Name the blood parasite species.
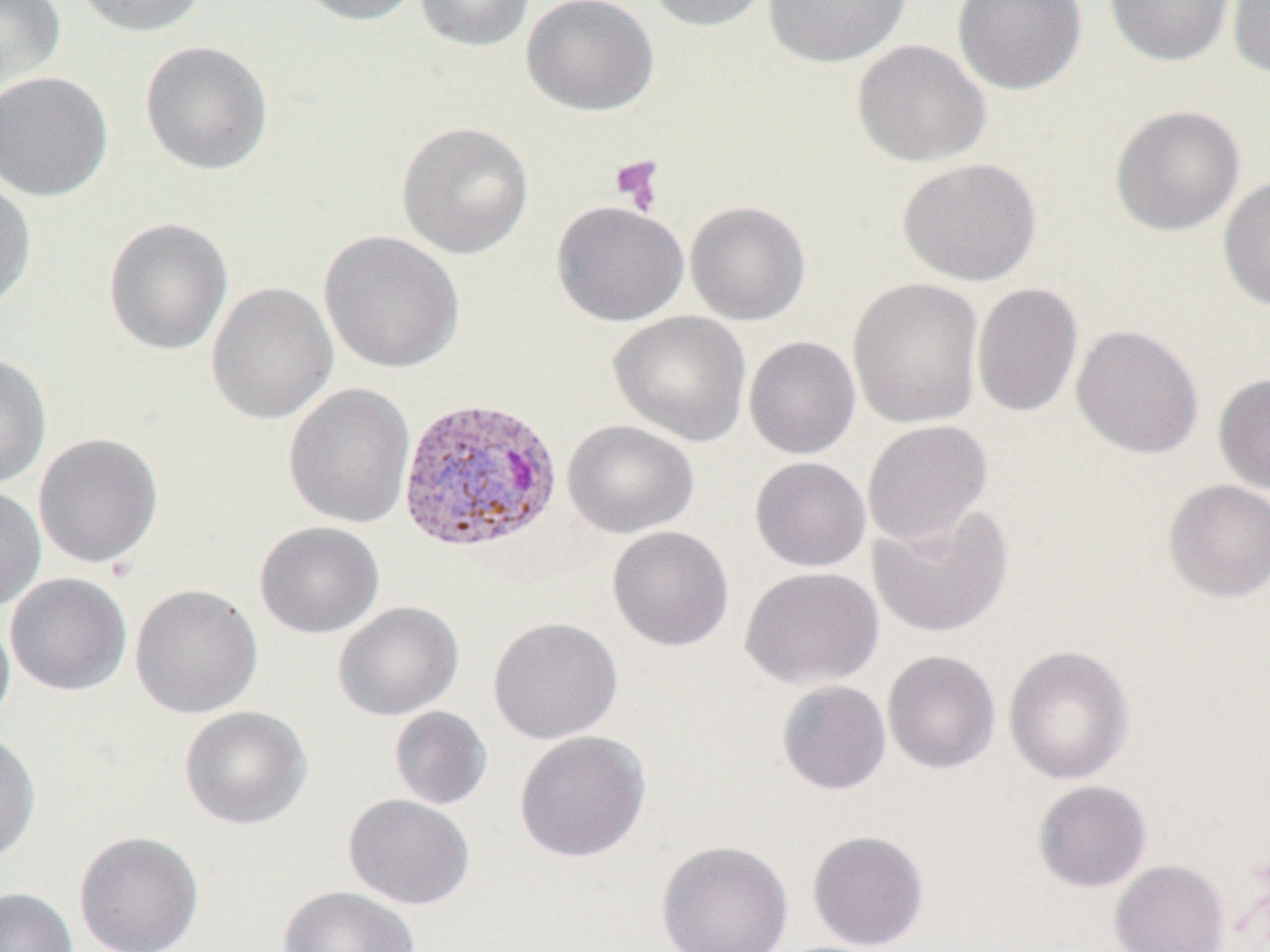
Plasmodium vivax.

Approximate bounding boxes as named x1/y1/x2/y2 corners in pixels. Plasmodium vivax-infected red blood cell locations: (x1=397, y1=396, x2=563, y2=553). Platelet locations: (x1=609, y1=155, x2=666, y2=214). Uninfected red blood cell locations: (x1=0, y1=0, x2=66, y2=95), (x1=71, y1=0, x2=211, y2=38), (x1=291, y1=0, x2=425, y2=26), (x1=415, y1=0, x2=535, y2=52), (x1=522, y1=0, x2=659, y2=115), (x1=642, y1=0, x2=772, y2=32), (x1=763, y1=0, x2=912, y2=68), (x1=952, y1=0, x2=1086, y2=94), (x1=1103, y1=0, x2=1235, y2=66), (x1=1227, y1=0, x2=1270, y2=79), (x1=851, y1=39, x2=991, y2=167), (x1=139, y1=40, x2=273, y2=175), (x1=0, y1=71, x2=113, y2=202), (x1=1110, y1=104, x2=1245, y2=236), (x1=396, y1=121, x2=534, y2=259), (x1=897, y1=157, x2=1041, y2=286), (x1=0, y1=173, x2=37, y2=313), (x1=1218, y1=175, x2=1270, y2=312), (x1=551, y1=200, x2=690, y2=327), (x1=685, y1=201, x2=811, y2=326), (x1=103, y1=217, x2=233, y2=356), (x1=319, y1=230, x2=465, y2=374), (x1=847, y1=277, x2=985, y2=429), (x1=205, y1=282, x2=338, y2=425), (x1=972, y1=282, x2=1083, y2=418), (x1=608, y1=310, x2=752, y2=446), (x1=1071, y1=325, x2=1204, y2=459), (x1=744, y1=335, x2=860, y2=459), (x1=0, y1=353, x2=51, y2=489), (x1=1213, y1=373, x2=1270, y2=494), (x1=283, y1=382, x2=416, y2=529), (x1=563, y1=420, x2=698, y2=538), (x1=862, y1=420, x2=992, y2=547), (x1=32, y1=433, x2=164, y2=569), (x1=750, y1=457, x2=871, y2=571), (x1=1162, y1=479, x2=1270, y2=602), (x1=0, y1=484, x2=46, y2=613), (x1=869, y1=504, x2=1014, y2=638), (x1=255, y1=521, x2=384, y2=639), (x1=607, y1=526, x2=734, y2=651), (x1=740, y1=566, x2=884, y2=689), (x1=4, y1=573, x2=132, y2=696), (x1=129, y1=584, x2=263, y2=718), (x1=333, y1=602, x2=464, y2=721), (x1=0, y1=611, x2=15, y2=729), (x1=488, y1=616, x2=623, y2=744), (x1=1003, y1=644, x2=1135, y2=785), (x1=882, y1=649, x2=1001, y2=774), (x1=776, y1=680, x2=892, y2=795), (x1=178, y1=706, x2=313, y2=830), (x1=389, y1=706, x2=492, y2=810), (x1=514, y1=730, x2=650, y2=862), (x1=0, y1=732, x2=42, y2=864), (x1=1032, y1=780, x2=1152, y2=893), (x1=343, y1=794, x2=475, y2=909), (x1=807, y1=829, x2=929, y2=951), (x1=73, y1=830, x2=204, y2=952), (x1=656, y1=840, x2=794, y2=951), (x1=1109, y1=859, x2=1229, y2=952), (x1=277, y1=885, x2=421, y2=952), (x1=0, y1=887, x2=79, y2=952). Image is 1270×952 pixels. Optical microscopy. 1000x magnification. Single field of view. Thin blood film. May-Grünwald-Giemsa-stained preparation.